Locate every Plasmodium parasite.
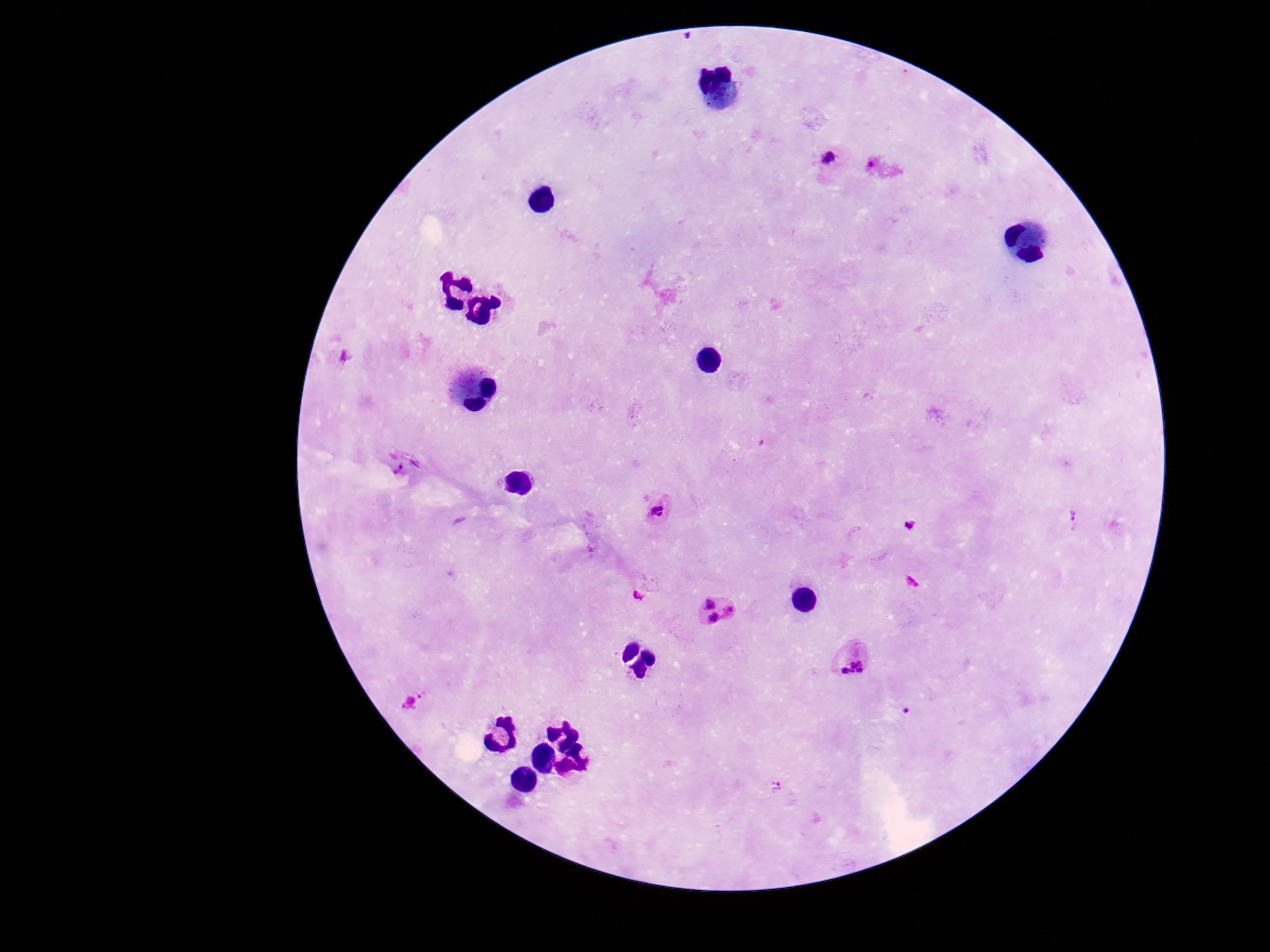
Approximate centers as (x, y) in pixels.
Plasmodium parasites: (830, 161), (406, 465), (659, 511), (1075, 519), (720, 611), (855, 658), (421, 696), (777, 789).

Summary:
  - Stain: Giemsa
  - Field of view: single
  - Magnification: 100x
  - Patient malaria status: infected
  - Image size: 1270×952 pixels
  - Preparation: thick blood smear
  - Capture: smartphone camera through the microscope eyepiece